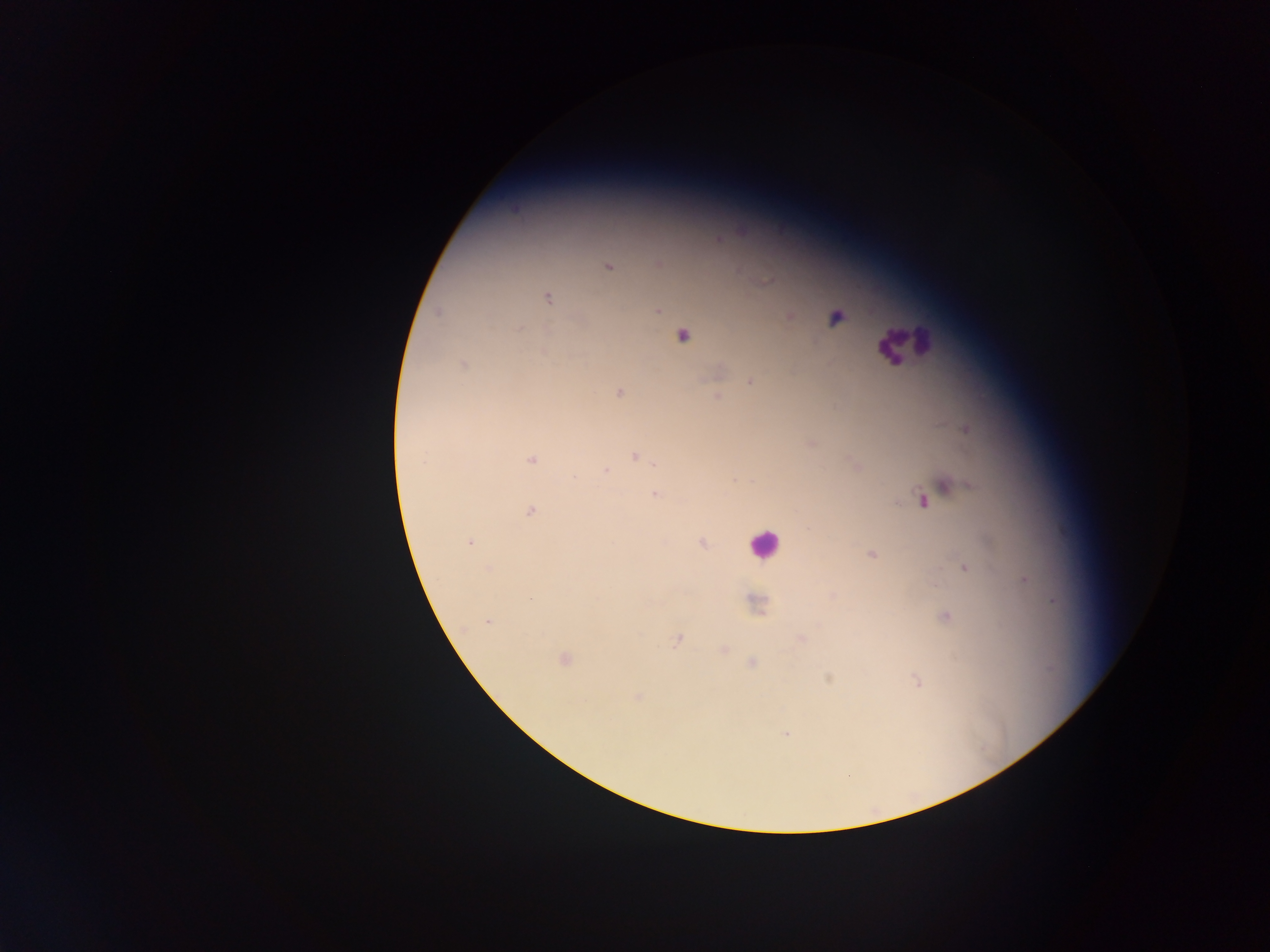

{
  "leukocyte_locations": "approximate centers as x y in pixels: 905 343; 764 545",
  "capture": "mobile-phone photograph through a microscope",
  "malaria_parasite_locations": "approximate centers as x y in pixels: 719 239; 660 264; 607 265; 766 280; 547 298; 657 310; 439 312; 789 316; 836 318; 517 328; 681 335; 543 352; 463 365; 751 381; 619 391; 717 396; 965 428; 810 442; 634 455; 531 460; 655 463; 857 466; 605 471; 734 479; 945 486; 655 494; 922 501; 530 511; 469 542; 701 542; 871 553; 964 567; 1026 579; 832 596; 756 604; 944 616; 487 621; 677 638; 800 639; 723 649; 564 659; 751 663; 828 677; 916 682; 638 696; 786 733",
  "preparation": "thick blood smear",
  "country": "Ghana",
  "field_of_view": "single",
  "image_size": "1270×952 pixels"
}